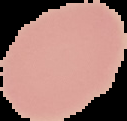

Summary:
  - Preparation: thin blood smear
  - Result: negative for malaria parasites
  - Image type: segmented cell region on a black background
  - Image size: 127×121 pixels